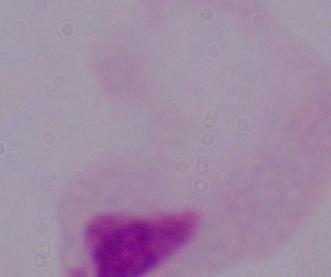
Summary:
  - Identification: trichomonad
  - Magnification: 1000x
  - Modality: photomicrograph